Locate and identify every blood parasite.
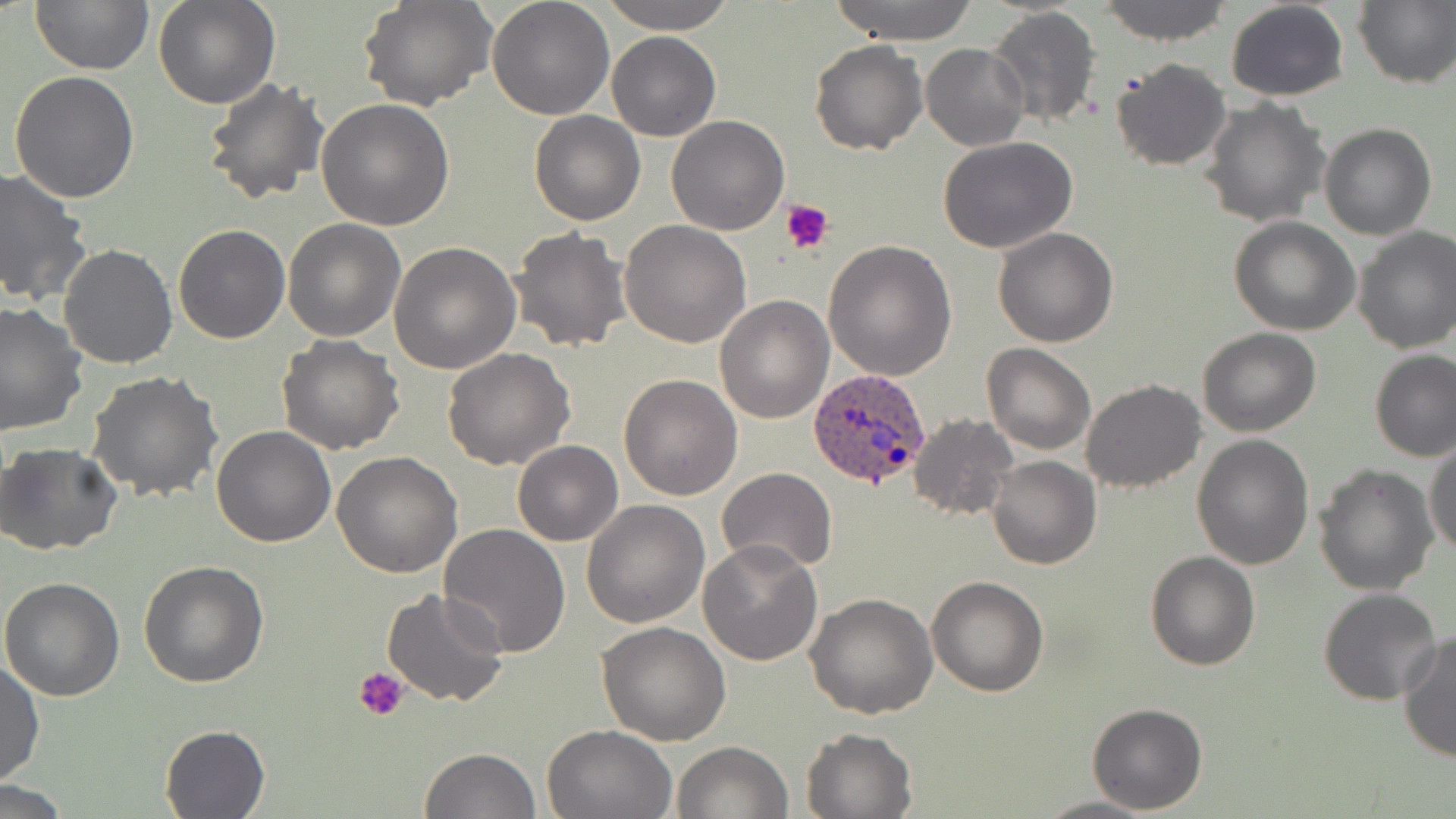
Approximate bounding boxes as (x1, y1, x2, y2) in pixels.
Plasmodium ovale-infected red blood cells: (808, 367, 931, 488).
No Plasmodium falciparum, Plasmodium malariae, Plasmodium vivax, Babesia divergens, or Trypanosoma brucei observed.

Platelet locations: (780, 197, 832, 254), (354, 665, 411, 723). Uninfected red blood cell locations: (30, 0, 154, 73), (153, 0, 280, 109), (358, 0, 496, 111), (488, 0, 615, 121), (598, 0, 737, 34), (826, 0, 985, 44), (1097, 0, 1232, 45), (1224, 1, 1349, 101), (1354, 2, 1455, 87), (986, 7, 1102, 128), (607, 32, 721, 141), (810, 37, 927, 154), (921, 42, 1030, 151), (1110, 58, 1234, 171), (9, 71, 140, 203), (202, 76, 329, 208), (1200, 97, 1330, 227), (317, 98, 458, 230), (529, 111, 645, 225), (666, 115, 788, 236), (1318, 123, 1435, 240), (937, 138, 1079, 253), (0, 169, 91, 307), (283, 218, 405, 342), (1229, 218, 1360, 335), (619, 221, 751, 350), (172, 225, 290, 344), (508, 226, 634, 352), (993, 227, 1120, 347), (1352, 227, 1456, 354), (825, 239, 956, 380), (389, 240, 521, 375), (59, 244, 177, 370), (715, 296, 834, 424), (0, 301, 89, 436), (1197, 327, 1323, 437), (276, 335, 405, 456), (981, 344, 1097, 456), (443, 346, 574, 470), (1370, 350, 1456, 461), (85, 369, 223, 502), (618, 373, 743, 500), (1081, 380, 1205, 493), (910, 414, 1018, 519), (211, 424, 338, 547), (1191, 434, 1314, 572), (1425, 439, 1456, 558), (513, 440, 623, 546), (1, 442, 124, 555), (331, 452, 462, 577), (987, 455, 1102, 570), (1313, 464, 1439, 596), (717, 467, 837, 573), (582, 500, 711, 628), (438, 522, 570, 660), (695, 540, 822, 665), (1145, 551, 1260, 671), (139, 560, 269, 686), (926, 575, 1050, 695), (0, 576, 126, 701), (381, 588, 510, 710), (1317, 588, 1443, 706), (805, 594, 937, 718), (596, 622, 731, 746), (1397, 631, 1456, 761), (1, 660, 44, 787), (1086, 702, 1207, 814), (541, 723, 677, 817), (158, 725, 270, 817), (802, 727, 916, 818), (672, 740, 792, 819), (419, 747, 542, 819), (0, 782, 76, 816), (1033, 794, 1162, 818). Slide-level diagnosis: Plasmodium ovale. May-Grünwald-Giemsa-stained preparation. Thin blood film. Single field of view. Image is 1456×819 pixels. Captured at 1000x magnification. Light microscopy.